Outline each blood parasite and name the species.
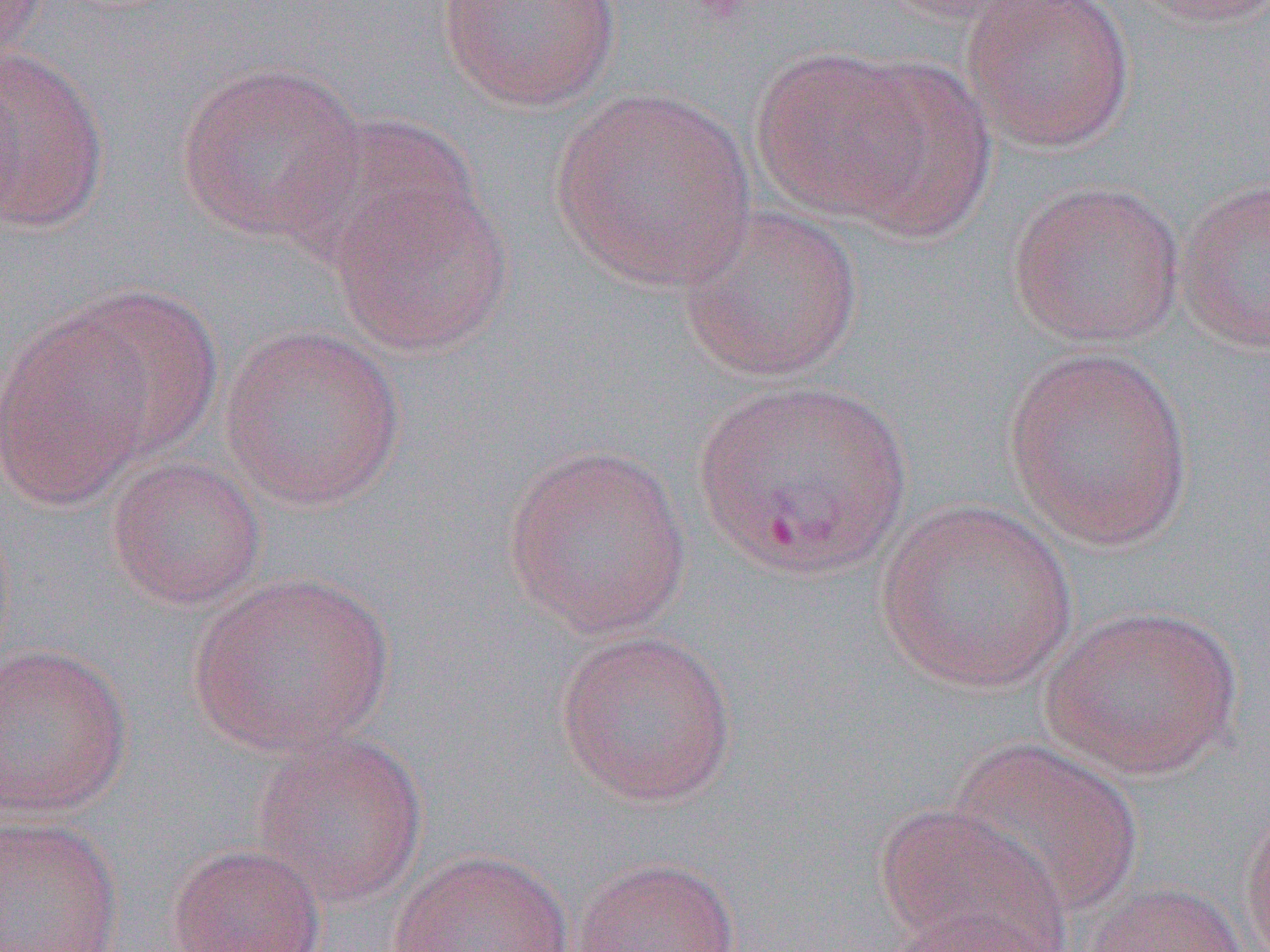
Approximate bounding boxes as named x1/y1/x2/y2 corners in pixels.
Plasmodium vivax-infected red blood cells: (x1=692, y1=374, x2=913, y2=582).
No Plasmodium falciparum, Plasmodium ovale, Plasmodium malariae, Babesia divergens, or Trypanosoma brucei observed.

Uninfected red blood cell locations: (x1=1, y1=0, x2=50, y2=64), (x1=434, y1=0, x2=623, y2=112), (x1=878, y1=0, x2=1052, y2=28), (x1=961, y1=0, x2=1136, y2=154), (x1=1124, y1=0, x2=1270, y2=30), (x1=0, y1=43, x2=111, y2=234), (x1=751, y1=46, x2=942, y2=224), (x1=829, y1=56, x2=996, y2=238), (x1=174, y1=61, x2=369, y2=244), (x1=550, y1=87, x2=756, y2=291), (x1=327, y1=174, x2=516, y2=358), (x1=1175, y1=175, x2=1270, y2=355), (x1=1005, y1=179, x2=1186, y2=349), (x1=674, y1=203, x2=865, y2=383), (x1=54, y1=285, x2=223, y2=460), (x1=0, y1=315, x2=157, y2=508), (x1=219, y1=324, x2=405, y2=512), (x1=1002, y1=344, x2=1194, y2=551), (x1=502, y1=442, x2=693, y2=640), (x1=105, y1=453, x2=267, y2=610), (x1=874, y1=499, x2=1080, y2=694), (x1=187, y1=570, x2=396, y2=758), (x1=1038, y1=605, x2=1243, y2=778), (x1=552, y1=627, x2=739, y2=808), (x1=0, y1=641, x2=134, y2=820), (x1=250, y1=732, x2=427, y2=908), (x1=946, y1=738, x2=1144, y2=917), (x1=1238, y1=797, x2=1270, y2=952), (x1=875, y1=804, x2=1071, y2=951), (x1=0, y1=813, x2=124, y2=951), (x1=166, y1=842, x2=327, y2=952), (x1=389, y1=848, x2=575, y2=952), (x1=570, y1=856, x2=743, y2=952), (x1=1078, y1=881, x2=1253, y2=952), (x1=875, y1=912, x2=1067, y2=952). Slide-level diagnosis: Plasmodium vivax. Light microscopy. Thin blood smear. 1000x magnification. Image is 1270×952 pixels. One field of a larger specimen.